Report the malaria status of this cell.
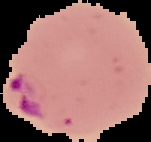

Parasitized.

From a thin blood film. Image is 151×142 pixels. The area outside the segmented cell region is set to black.